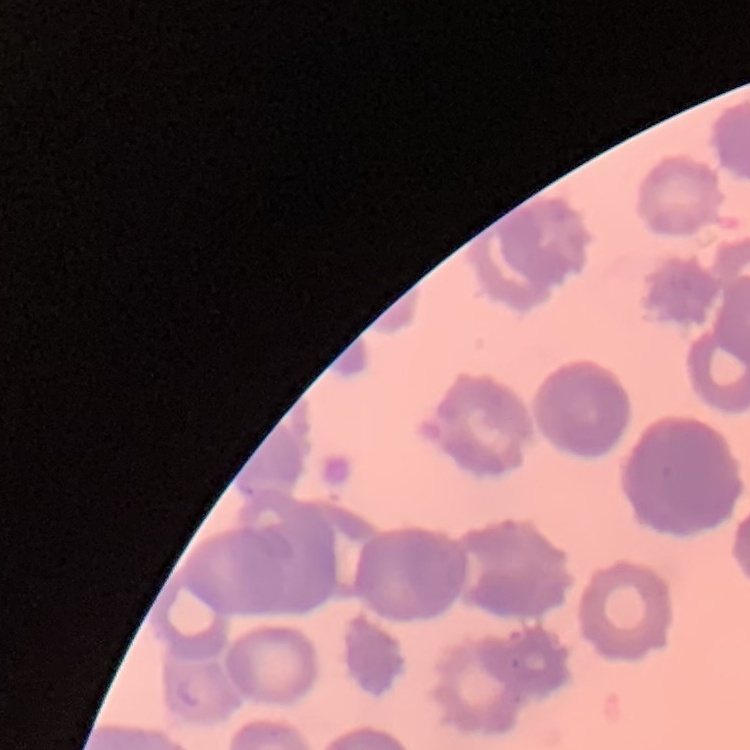
Summary:
  - Red blood cell morphology: rouleaux formation
  - Stain: Field's or Giemsa
  - Preparation: thin peripheral smear
  - Image type: one tile cut from a larger photomicrograph